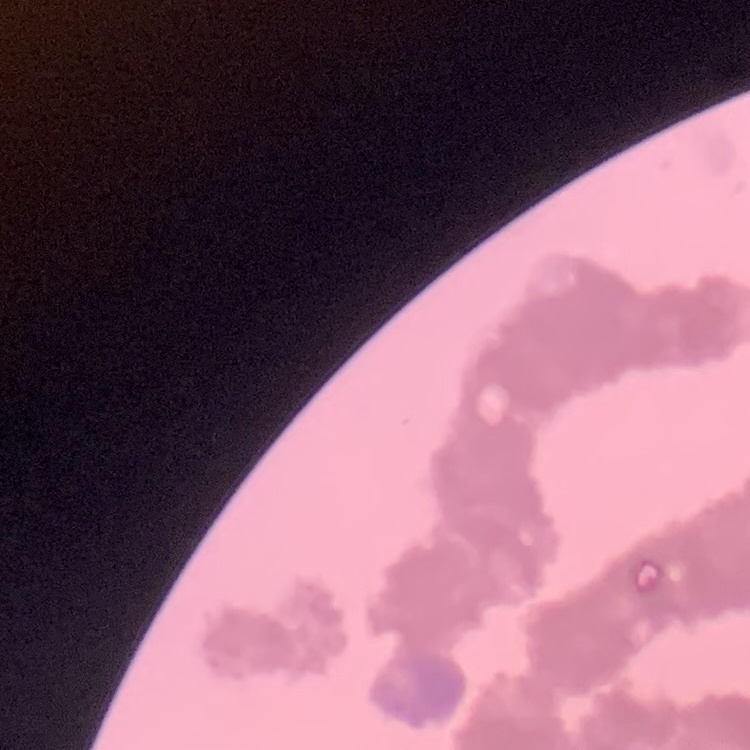 The erythrocytes show rouleaux formation. One tile cut from a larger photomicrograph. Field's or Giemsa stain. Thin peripheral smear.